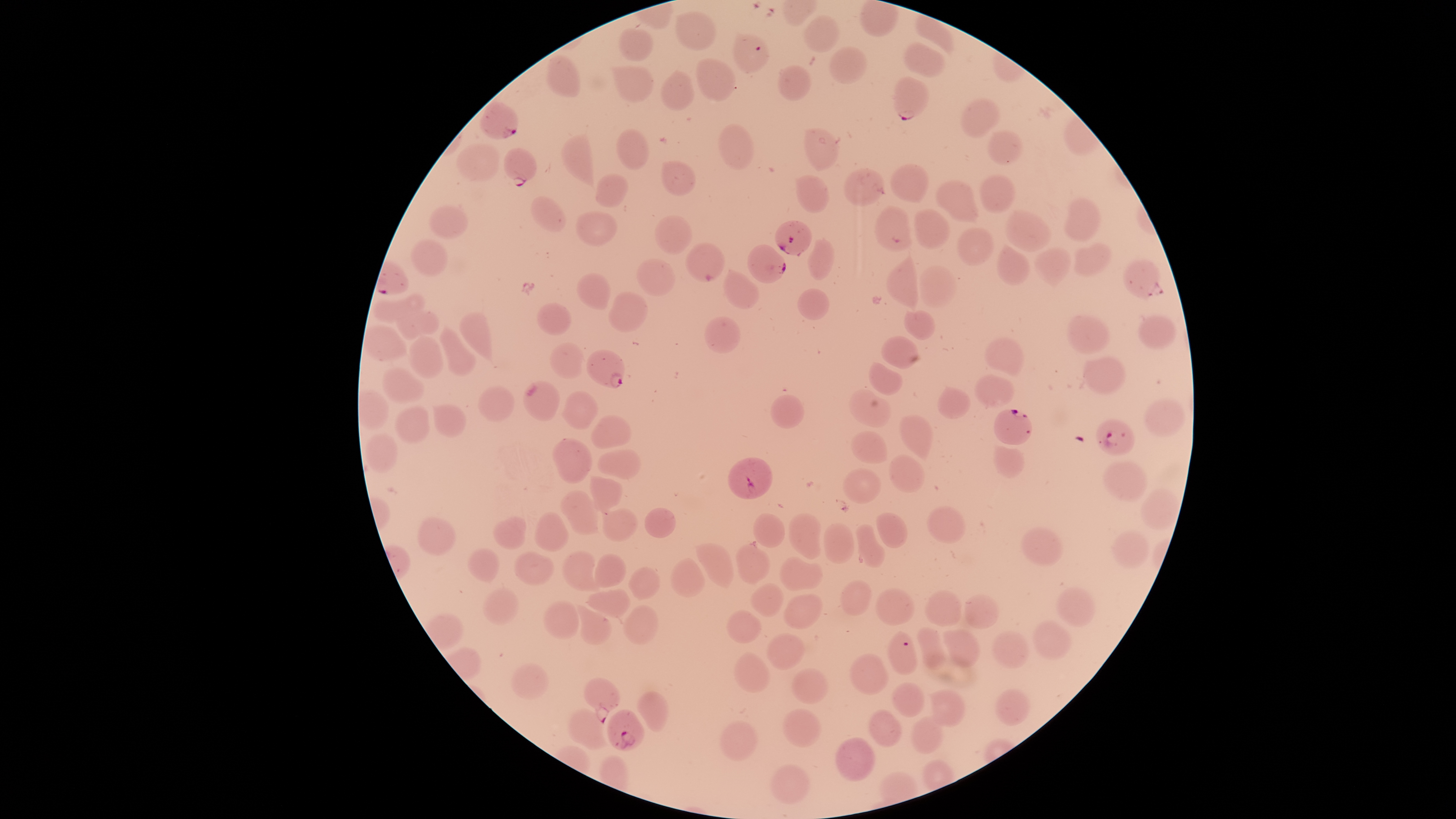

{
  "visible_region": "circular",
  "uninfected_red_blood_cells": "approximate bounding boxes as [left, top, right, bottom] in pixels: [675, 10, 717, 50], [913, 13, 955, 58], [803, 14, 840, 53], [619, 27, 653, 62], [905, 41, 946, 77], [828, 46, 867, 84], [545, 53, 581, 98], [696, 58, 737, 102], [777, 65, 812, 101], [611, 66, 654, 103], [660, 70, 696, 111], [961, 97, 1000, 138], [717, 122, 754, 170], [803, 126, 840, 173], [614, 128, 649, 170], [560, 130, 595, 190], [986, 130, 1024, 166], [455, 143, 501, 183], [660, 159, 699, 197], [888, 163, 930, 203], [842, 167, 885, 207], [595, 172, 630, 208], [978, 173, 1015, 213], [794, 174, 831, 213], [934, 179, 979, 223], [530, 195, 568, 232], [1063, 197, 1101, 243], [428, 205, 470, 240], [874, 205, 912, 253], [914, 208, 950, 250], [1005, 209, 1053, 252], [574, 210, 619, 247], [654, 215, 694, 255], [956, 227, 995, 266], [807, 236, 836, 281], [410, 238, 448, 278], [1073, 241, 1113, 277], [685, 242, 726, 283], [996, 243, 1031, 286], [1033, 247, 1072, 288], [885, 256, 919, 320], [636, 257, 676, 297], [919, 264, 957, 308], [724, 269, 760, 309], [576, 271, 611, 310], [797, 287, 830, 321], [371, 291, 426, 322], [607, 291, 650, 332], [537, 301, 572, 336], [395, 309, 440, 340], [904, 309, 937, 340], [458, 310, 493, 365], [1137, 313, 1178, 349], [1065, 314, 1110, 355], [704, 315, 741, 354], [363, 324, 409, 361], [438, 324, 478, 377], [408, 334, 443, 379], [880, 335, 918, 370], [983, 335, 1024, 378], [550, 342, 585, 380], [1082, 356, 1126, 396], [868, 362, 903, 396], [382, 366, 425, 404], [974, 373, 1015, 408], [523, 380, 561, 421], [477, 385, 515, 422], [936, 385, 972, 419], [848, 388, 892, 428], [560, 391, 599, 430], [770, 394, 804, 429], [1143, 398, 1186, 437], [395, 404, 430, 445], [432, 405, 467, 438], [590, 414, 632, 449], [899, 414, 933, 460], [851, 431, 888, 464], [365, 433, 399, 472], [551, 438, 593, 484], [992, 445, 1025, 478], [597, 449, 641, 479], [889, 454, 925, 493], [1102, 460, 1149, 501], [842, 468, 881, 503], [589, 473, 624, 515], [1140, 487, 1181, 532], [559, 490, 600, 535], [926, 506, 966, 545], [602, 507, 639, 542], [644, 507, 676, 538], [534, 511, 569, 552], [876, 512, 908, 548], [752, 513, 785, 548], [788, 513, 822, 560], [416, 516, 457, 555], [493, 516, 528, 550], [823, 522, 855, 564], [856, 523, 885, 568], [1020, 525, 1064, 566], [1111, 530, 1151, 569], [695, 543, 733, 590], [734, 543, 771, 585], [467, 547, 500, 585], [513, 550, 554, 585], [561, 551, 601, 592], [593, 553, 627, 587], [779, 556, 824, 591], [669, 557, 705, 598], [627, 566, 660, 600], [840, 579, 872, 617], [750, 582, 784, 617], [481, 586, 519, 625], [1053, 586, 1096, 627], [585, 587, 631, 619], [875, 587, 916, 625], [923, 590, 962, 628], [784, 593, 824, 629], [964, 593, 999, 629], [543, 600, 579, 639], [574, 603, 611, 645], [622, 604, 658, 645], [726, 610, 763, 644], [1032, 618, 1073, 661], [916, 626, 947, 671], [942, 630, 981, 669], [990, 630, 1029, 669], [766, 631, 805, 670], [733, 651, 771, 693], [849, 652, 890, 695], [790, 668, 828, 704], [890, 681, 926, 717], [994, 687, 1032, 726], [927, 688, 967, 727], [637, 690, 670, 732], [782, 706, 821, 747], [566, 707, 612, 750], [867, 708, 903, 747], [910, 714, 944, 754], [719, 719, 759, 761], [834, 737, 876, 782], [769, 764, 810, 804]",
  "parasitized_red_blood_cells": "approximate bounding boxes as [left, top, right, bottom] in pixels: [732, 32, 770, 74], [893, 76, 930, 121], [479, 100, 519, 140], [502, 147, 538, 188], [774, 220, 813, 257], [747, 244, 787, 283], [1122, 257, 1161, 300], [586, 349, 625, 389], [993, 409, 1033, 445], [1094, 418, 1135, 456], [727, 456, 773, 498], [887, 630, 918, 675], [583, 677, 620, 724], [607, 710, 646, 750]",
  "presence": "malaria parasites seen",
  "stain": "Giemsa",
  "field_of_view": "single",
  "capture": "smartphone photograph through the microscope eyepiece",
  "image_size": "1456×819 pixels",
  "species": "Plasmodium falciparum",
  "preparation": "thin blood smear"
}